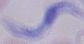 Photomicrograph. 1000x magnification. A trypanosome is shown.